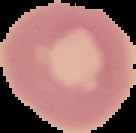
Summary:
  - Image type: segmented cell region with the area outside set to black
  - Result: no Plasmodium parasites seen
  - Preparation: thin blood smear
  - Image size: 136×133 pixels